Classify this cell by malaria status.
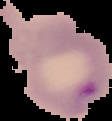

It is parasitized.

Cell region segmented out of the field of view; the surrounding area is masked to black. From a thin blood smear. Image is 112×121 pixels.